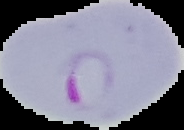
image size = 184×130 pixels
preparation = thin blood smear
image type = segmented cell region on a black background
result = Plasmodium parasites detected